Locate every parasitized red blood cell.
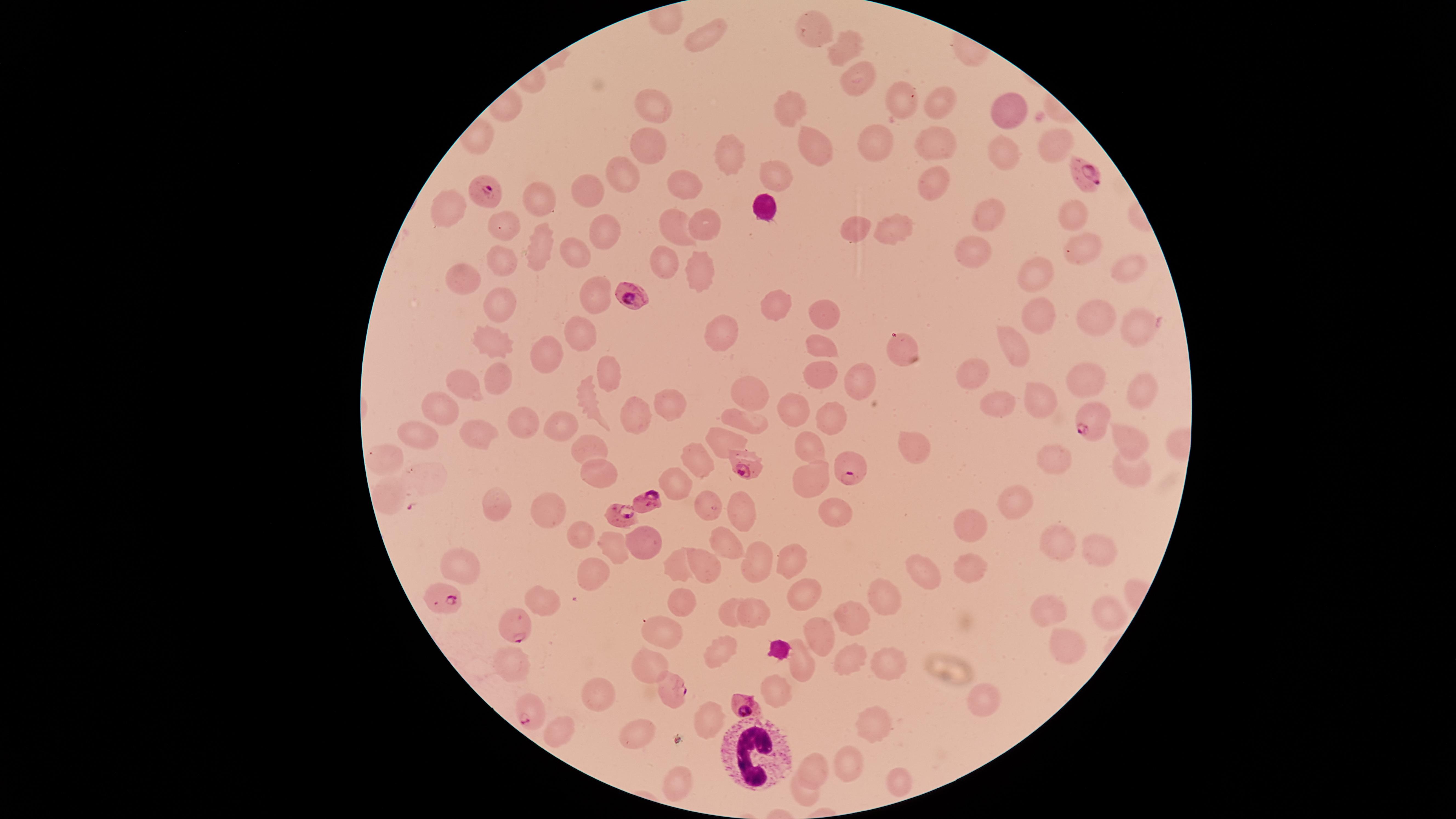
Approximate marker points as {x, y} in pixels.
Parasitized red blood cells: {1084, 179}, {483, 190}, {631, 294}, {1090, 421}, {747, 464}, {852, 468}, {646, 503}, {618, 514}, {439, 598}, {514, 627}, {675, 687}, {744, 704}, {526, 709}.

visible_region: circular
image_size: 1456×819 pixels
white_blood_cells: 'approximate marker points as {x, y} in pixels: {762, 207}, {747, 750}'
field_of_view: single
species: Plasmodium falciparum
stain: Giemsa
capture: smartphone photograph through the microscope eyepiece
preparation: thin blood film
uninfected_red_blood_cells: 'approximate marker points as {x, y} in pixels: {812, 33}, {699, 37}, {844, 43}, {851, 79}, {902, 96}, {939, 103}, {790, 107}, {656, 110}, {1014, 111}, {880, 141}, {935, 141}, {811, 143}, {1054, 146}, {653, 147}, {728, 153}, {1003, 154}, {775, 175}, {616, 179}, {934, 183}, {688, 190}, {584, 193}, {541, 198}, {452, 201}, {988, 213}, {1074, 214}, {504, 222}, {671, 226}, {890, 227}, {707, 229}, {856, 229}, {603, 237}, {537, 246}, {1080, 246}, {972, 250}, {572, 252}, {663, 262}, {498, 265}, {1125, 265}, {694, 275}, {462, 277}, {1034, 277}, {592, 297}, {497, 305}, {778, 308}, {826, 313}, {1037, 316}, {1095, 317}, {1136, 330}, {721, 334}, {577, 335}, {494, 339}, {1014, 346}, {822, 347}, {899, 347}, {543, 355}, {971, 371}, {819, 374}, {1083, 377}, {607, 378}, {857, 378}, {500, 380}, {467, 385}, {1142, 386}, {751, 389}, {1037, 393}, {586, 400}, {1000, 402}, {669, 403}, {792, 408}, {432, 409}, {830, 415}, {633, 416}, {517, 423}, {747, 424}, {563, 425}, {476, 435}, {413, 439}, {725, 439}, {1127, 441}, {589, 444}, {915, 445}, {809, 446}, {1059, 457}, {703, 461}, {385, 462}, {1125, 471}, {599, 473}, {425, 475}, {674, 482}, {808, 486}, {1018, 496}, {385, 497}, {494, 507}, {549, 507}, {710, 507}, {740, 511}, {834, 511}, {972, 522}, {578, 533}, {645, 540}, {606, 543}, {723, 544}, {1055, 548}, {1097, 556}, {785, 559}, {759, 561}, {969, 561}, {678, 564}, {924, 566}, {701, 567}, {467, 568}, {595, 575}, {803, 595}, {544, 600}, {680, 602}, {880, 602}, {727, 609}, {1050, 611}, {757, 615}, {1109, 617}, {849, 620}, {664, 632}, {822, 635}, {1065, 648}, {719, 652}, {852, 660}, {512, 664}, {803, 664}, {888, 664}, {653, 667}, {602, 696}, {776, 696}, {982, 703}, {872, 720}, {705, 721}, {560, 730}, {639, 736}, {844, 764}, {812, 768}, {895, 781}, {678, 783}, {803, 794}'